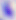
Photomicrograph. Toxoplasma gondii is seen. Captured at 400x magnification.